Report the malaria status of this cell.
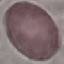

It is uninfected.

Thin blood smear. Photographed with a smartphone camera at the microscope eyepiece. Giemsa-stained preparation. Automatically extracted cell patch, resized to 64 × 64 pixels.